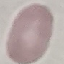
Result: negative for malaria parasites. Automatically extracted cell patch, resized to 64 × 64 pixels. Thin blood film. Giemsa-stained preparation. Photographed with a smartphone camera at the microscope eyepiece.